Identify the preparation type.
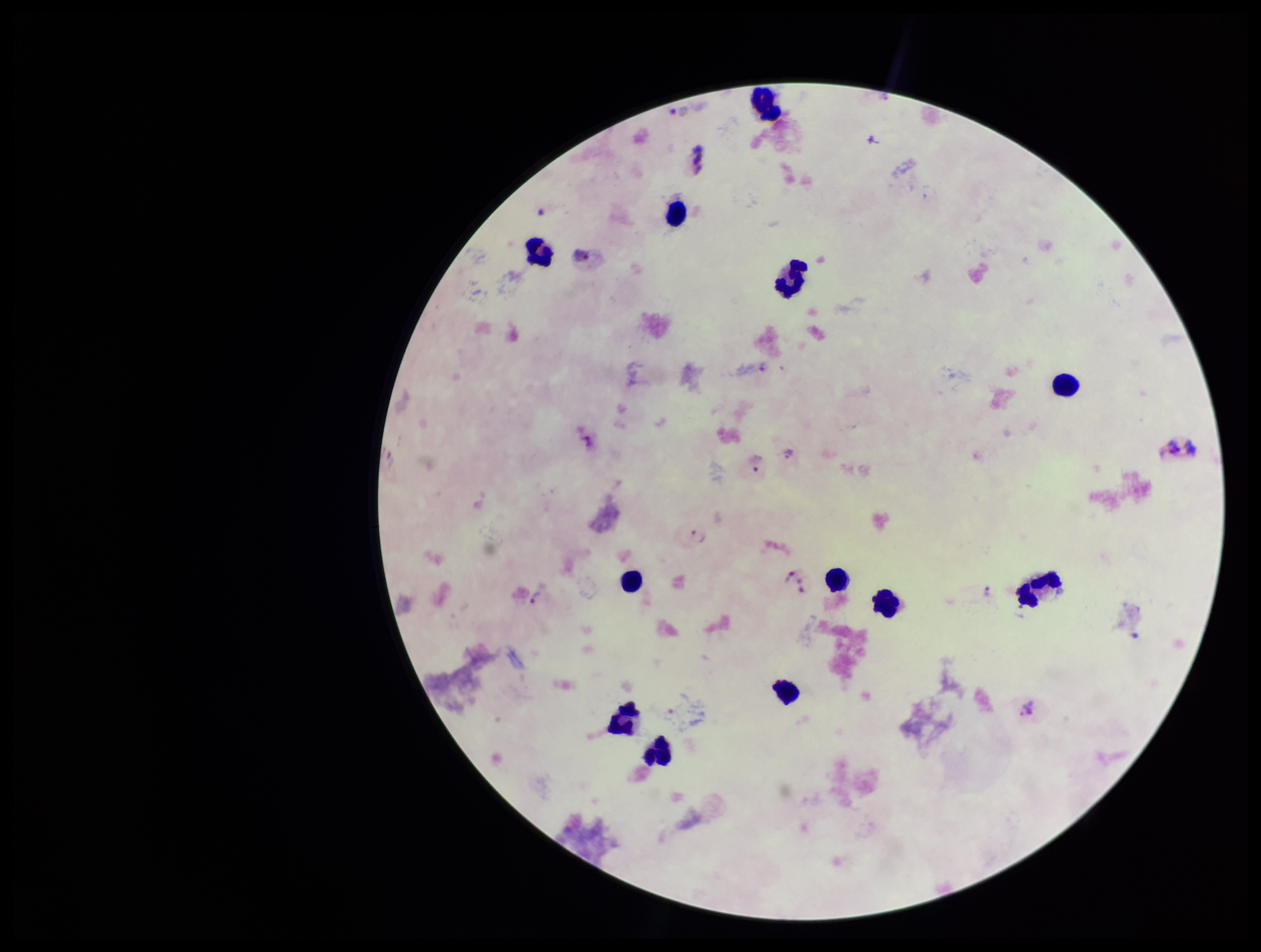

It is a thick blood smear.

Plasmodium parasites: seen. Species reported for this patient: Plasmodium vivax. Patient malaria status: positive. Photographed through the microscope eyepiece with a smartphone camera. Parasite count: 9. One field from this slide. Giemsa stain. Leukocyte count: 12. Image is 1261×952 pixels.